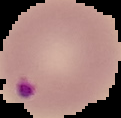 Cell region segmented out of the field of view; the surrounding area is masked to black. Image is 121×118 pixels. Result: Plasmodium parasites detected. From a thin blood film.